Locate and identify every blood parasite.
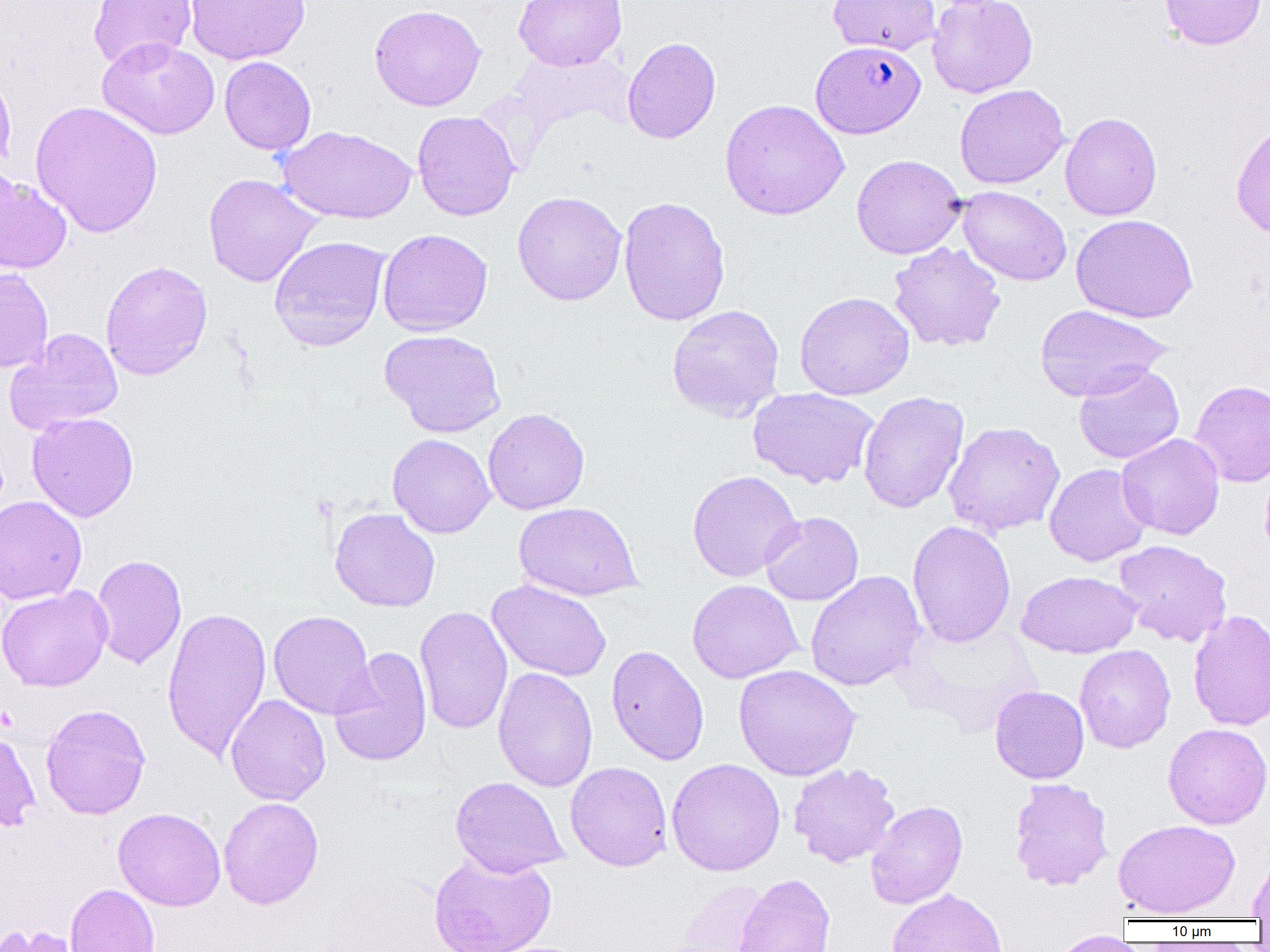

Approximate bounding boxes as (x1,y1)-(x2,y2) corner pairs in pixels.
Plasmodium falciparum-infected red blood cells: (810,40)-(926,139).
No Plasmodium ovale, Plasmodium malariae, Plasmodium vivax, Babesia divergens, or Trypanosoma brucei observed.

Summary:
  - Uninfected red blood cell locations: (88,0)-(197,70), (185,0)-(310,64), (513,0)-(627,71), (827,0)-(941,56), (927,0)-(1038,98), (1159,0)-(1267,51), (368,4)-(486,112), (97,36)-(220,140), (622,37)-(721,144), (219,56)-(316,155), (0,62)-(17,176), (954,84)-(1070,189), (719,99)-(850,220), (30,100)-(163,239), (412,111)-(520,221), (1059,112)-(1162,220), (1230,119)-(1270,240), (277,125)-(417,224), (851,154)-(965,259), (0,169)-(72,275), (203,173)-(323,288), (957,186)-(1072,286), (512,191)-(627,306), (618,195)-(731,326), (1071,214)-(1198,322), (377,228)-(493,336), (269,235)-(391,351), (887,242)-(1006,352), (100,260)-(213,380), (0,267)-(53,373), (795,291)-(915,400), (666,304)-(785,421), (1034,304)-(1171,401), (5,328)-(124,435), (379,329)-(506,438), (1074,363)-(1184,465), (1190,379)-(1270,487), (748,387)-(879,489), (858,391)-(969,513), (482,408)-(590,515), (27,411)-(139,522), (943,421)-(1065,538), (1116,433)-(1225,540), (387,434)-(495,538), (1044,463)-(1152,567), (686,469)-(802,582), (0,495)-(87,605), (513,502)-(642,601), (329,507)-(440,612), (760,511)-(863,606), (907,520)-(1016,647), (1113,539)-(1232,647), (90,554)-(187,669), (805,570)-(925,691), (1016,570)-(1141,658), (487,579)-(612,682), (687,579)-(803,683), (0,585)-(112,692), (414,605)-(513,735), (162,606)-(272,763), (1187,609)-(1270,731), (268,610)-(376,720), (1074,644)-(1176,753), (606,645)-(709,766), (329,646)-(432,767), (733,664)-(861,781), (493,667)-(598,792), (990,685)-(1090,783), (225,694)-(331,805), (40,703)-(151,820), (1163,723)-(1270,829), (0,727)-(41,833), (666,758)-(786,876), (565,761)-(673,871), (788,762)-(901,868), (450,776)-(568,878), (1008,778)-(1113,891), (218,797)-(324,909), (865,800)-(968,909), (113,807)-(226,911), (1114,819)-(1240,919), (1247,849)-(1270,921), (428,851)-(556,952), (732,873)-(836,952), (670,879)-(770,951), (65,883)-(160,952), (887,888)-(1007,952), (0,923)-(80,952), (1047,930)-(1139,952)
  - Slide-level diagnosis: Plasmodium falciparum
  - Magnification: 1000x
  - Image size: 1270×952 pixels
  - Field of view: one of a larger specimen
  - Preparation: thin blood smear
  - Modality: light microscopy